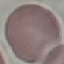

Malaria status: uninfected. Cell patch, automatically extracted from a larger field of view and resized to 64 × 64 pixels. Thin blood film. Giemsa-stained preparation. Acquired by smartphone through the microscope eyepiece.